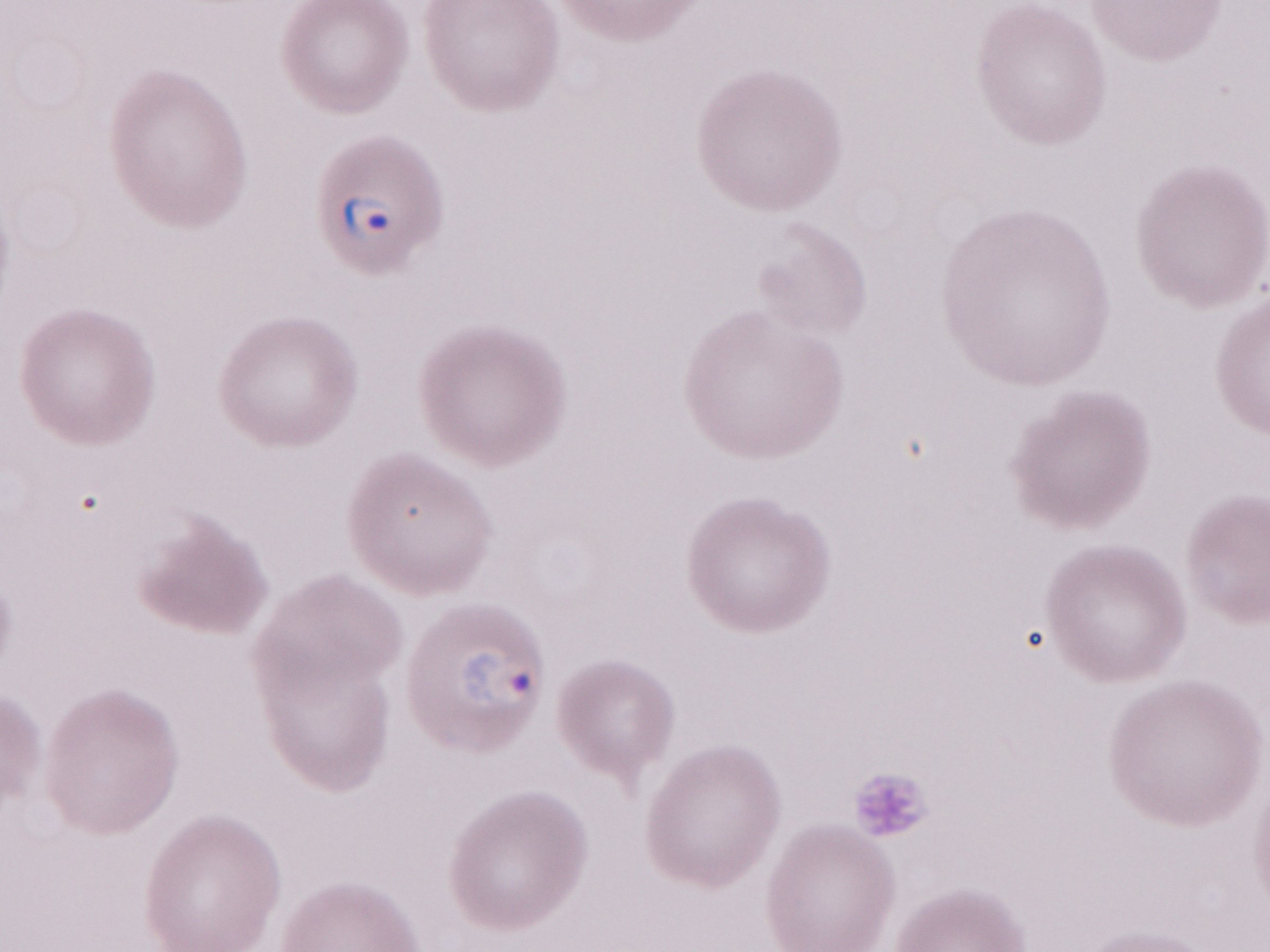 Thin peripheral-blood smear. Single field of view. Image is 1270×952 pixels. Patient diagnosis: malaria infection. May-Grünwald-Giemsa stain. 1,000x magnification. Olympus BX43 microscope, Olympus DP73 camera.